Name the cell type shown.
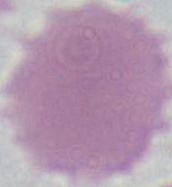

An erythrocyte.

Summary:
  - Modality: micrograph
  - Magnification: 1000x